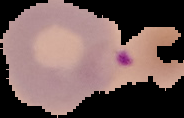

From a thin blood film. Result: malaria parasites detected. Cell region segmented out of the field of view; the surrounding area is masked to black. Image is 184×118 pixels.